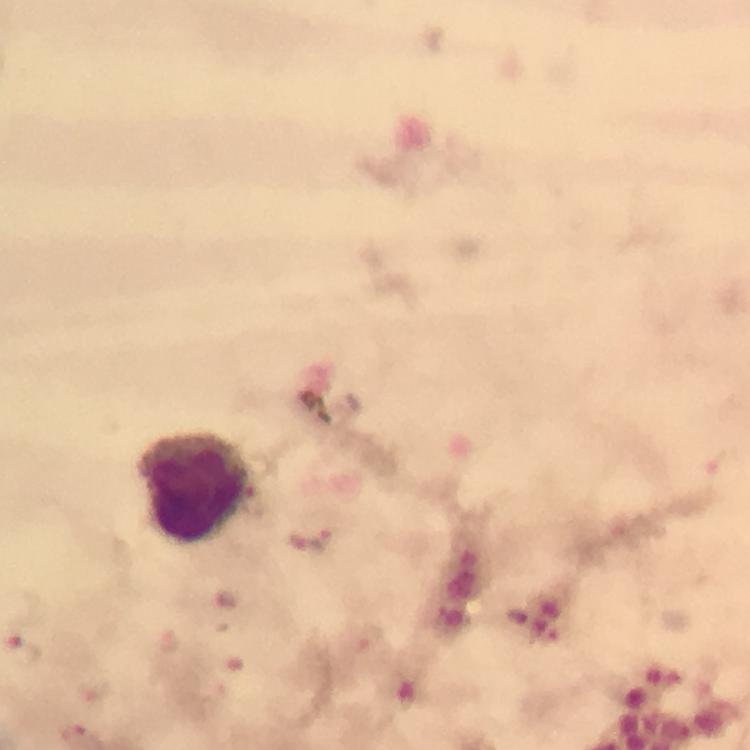
Approximate centers as (x, y) in pixels.
Summary:
  - Leukocyte locations: (195, 488)
  - Plasmodium parasite locations: (23, 650)
  - Immersion oil: applied
  - Cropped from: one field of view
  - Magnification: 100x
  - Context: from a diagnostic examination for malaria
  - Stain: Giemsa
  - Image size: 750×750 pixels
  - Preparation: thick blood smear
  - Capture: smartphone photograph through a microscope